Name the parasite shown.
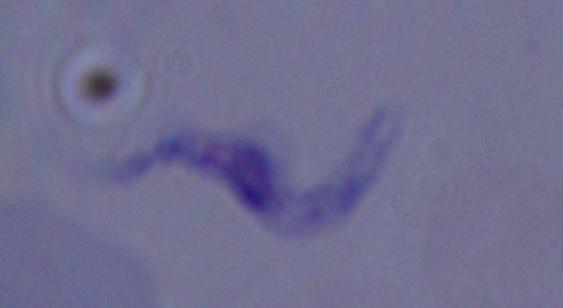

A trypanosome.

Captured at 1000x magnification. Micrograph.